Name the blood parasite species.
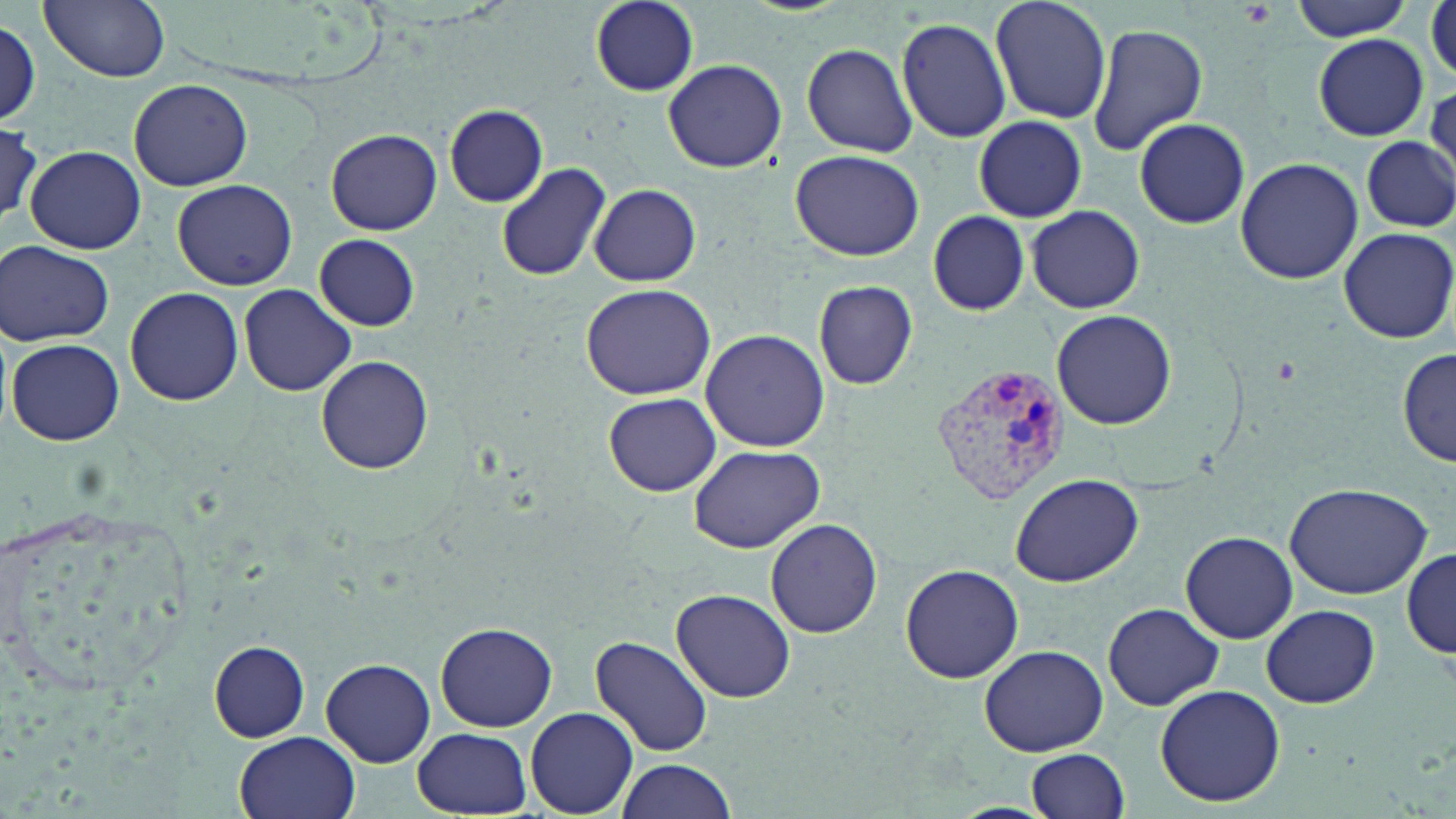
Plasmodium vivax.

Summary:
  - Coordinate format: approximate bounding boxes as (x1, y1, x2, y2) in pixels
  - Plasmodium vivax-infected red blood cell locations: (936, 364, 1073, 504)
  - Uninfected red blood cell locations: (41, 0, 171, 83), (590, 0, 699, 95), (991, 0, 1111, 124), (1290, 0, 1418, 40), (1427, 0, 1456, 84), (1, 18, 42, 122), (896, 18, 1012, 141), (1086, 20, 1209, 156), (1315, 36, 1429, 139), (799, 41, 920, 157), (662, 59, 787, 173), (128, 77, 256, 190), (445, 105, 548, 207), (972, 115, 1087, 222), (0, 117, 46, 229), (1134, 117, 1250, 230), (325, 129, 442, 236), (1360, 137, 1455, 231), (24, 145, 146, 254), (790, 148, 924, 262), (1235, 157, 1363, 284), (495, 162, 613, 283), (171, 180, 298, 289), (587, 184, 705, 286), (1025, 205, 1145, 313), (926, 211, 1030, 315), (1339, 227, 1456, 343), (314, 234, 420, 331), (1, 239, 117, 347), (813, 280, 918, 390), (579, 282, 717, 401), (238, 284, 357, 396), (125, 288, 245, 405), (1051, 310, 1176, 429), (700, 329, 830, 453), (7, 338, 124, 446), (1398, 348, 1455, 467), (316, 356, 433, 474), (600, 392, 726, 497), (687, 442, 827, 552), (1010, 473, 1144, 587), (1283, 482, 1432, 601), (766, 519, 883, 640), (1180, 531, 1297, 644), (1402, 548, 1455, 659), (899, 563, 1024, 683), (670, 588, 796, 703), (1103, 602, 1222, 711), (1261, 604, 1380, 709), (436, 622, 557, 730), (589, 635, 714, 759), (209, 640, 310, 742), (978, 644, 1108, 755), (320, 657, 435, 767), (1154, 684, 1286, 808), (527, 707, 637, 817), (412, 726, 534, 816), (234, 731, 360, 819), (1025, 747, 1132, 819), (611, 758, 741, 818)
  - Platelet locations: (1241, 1, 1275, 25)
  - Modality: optical microscopy
  - Preparation: thin blood smear
  - Magnification: 1000x
  - Field of view: one of a larger specimen
  - Stain: May-Grünwald-Giemsa
  - Image size: 1456×819 pixels